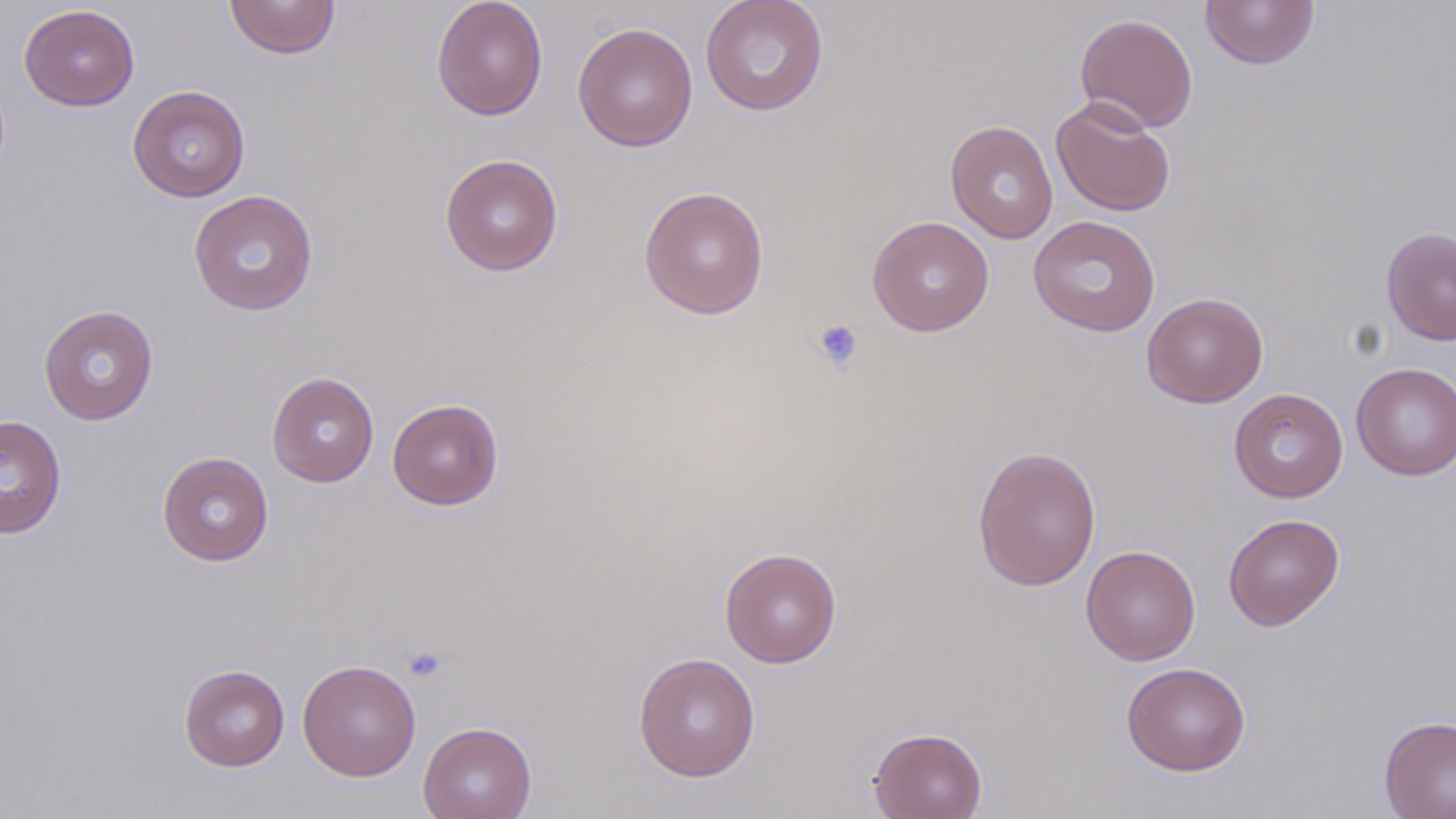 Approximate bounding boxes as named x1/y1/x2/y2 corners in pixels. Uninfected red blood cell locations: (x1=224, y1=0, x2=341, y2=59), (x1=431, y1=0, x2=548, y2=121), (x1=700, y1=0, x2=829, y2=116), (x1=1201, y1=0, x2=1320, y2=70), (x1=19, y1=5, x2=140, y2=111), (x1=1074, y1=13, x2=1198, y2=133), (x1=572, y1=21, x2=698, y2=152), (x1=127, y1=84, x2=250, y2=202), (x1=1050, y1=97, x2=1176, y2=217), (x1=945, y1=120, x2=1058, y2=244), (x1=440, y1=153, x2=563, y2=276), (x1=639, y1=186, x2=769, y2=319), (x1=188, y1=189, x2=319, y2=316), (x1=1028, y1=214, x2=1161, y2=337), (x1=867, y1=215, x2=994, y2=336), (x1=1381, y1=226, x2=1456, y2=346), (x1=1141, y1=292, x2=1268, y2=408), (x1=38, y1=304, x2=159, y2=425), (x1=1351, y1=362, x2=1456, y2=480), (x1=267, y1=371, x2=379, y2=487), (x1=1228, y1=387, x2=1349, y2=503), (x1=387, y1=398, x2=503, y2=510), (x1=0, y1=415, x2=67, y2=539), (x1=972, y1=445, x2=1102, y2=591), (x1=157, y1=451, x2=274, y2=566), (x1=1223, y1=513, x2=1345, y2=631), (x1=1081, y1=544, x2=1201, y2=665), (x1=719, y1=547, x2=842, y2=668), (x1=633, y1=652, x2=761, y2=782), (x1=297, y1=659, x2=421, y2=781), (x1=1121, y1=661, x2=1251, y2=776), (x1=179, y1=664, x2=290, y2=771), (x1=1378, y1=715, x2=1456, y2=819), (x1=418, y1=721, x2=537, y2=819), (x1=868, y1=726, x2=987, y2=819). Platelet locations: (x1=811, y1=319, x2=863, y2=371), (x1=402, y1=646, x2=448, y2=683). Slide-level diagnosis: negative for blood parasites. Thin blood film. Single field of view. Image is 1456×819 pixels. 1000x magnification. Light microscopy. May-Grünwald-Giemsa stain.